Look for parasitized red blood cells.
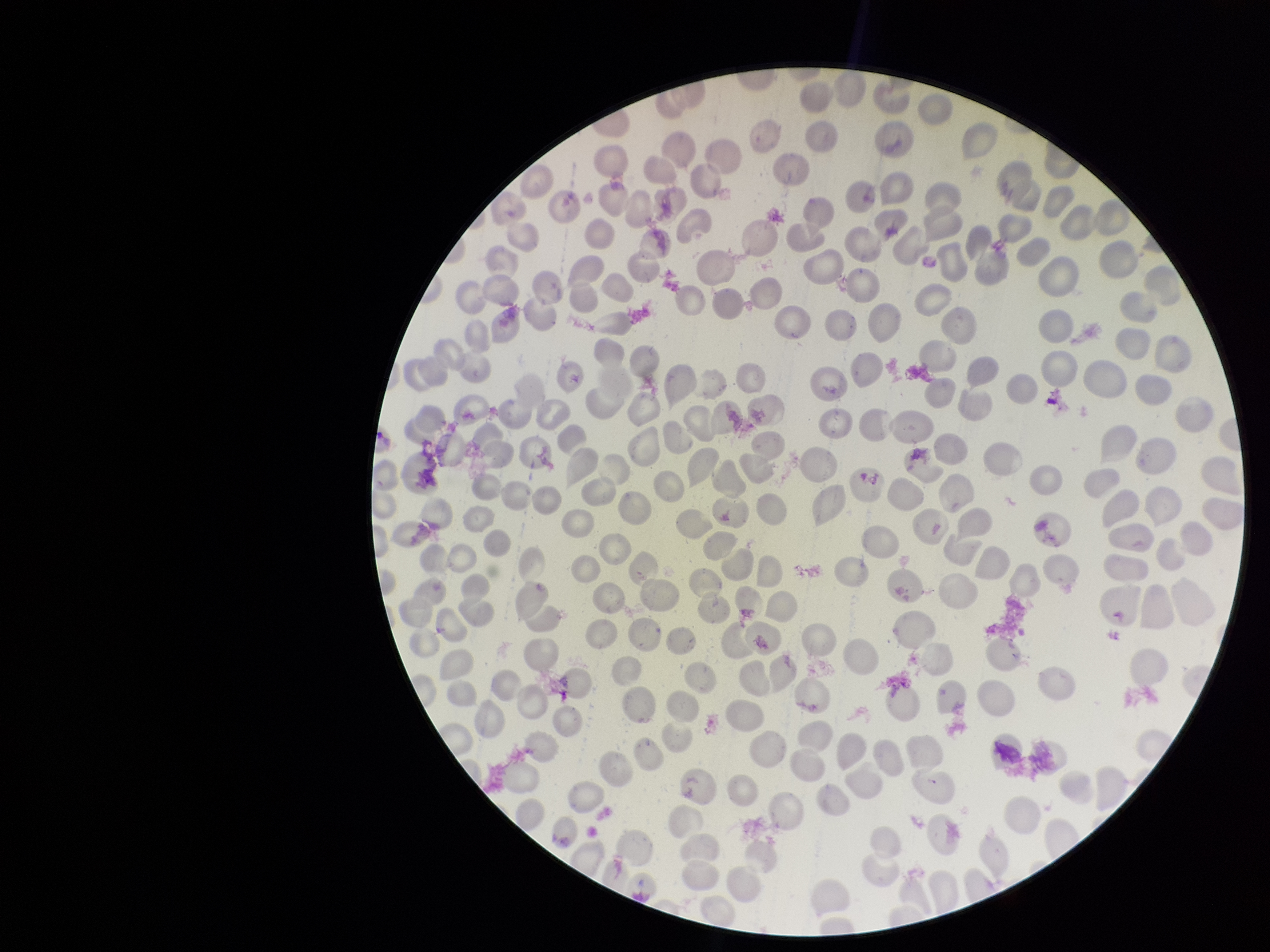

None seen.

stain = Giemsa
preparation = thin blood smear
image size = 1270×952 pixels
patient malaria status = positive
red blood cell count = 268
capture = smartphone photograph through the microscope eyepiece
parasitized red blood cell count = 0
species reported for this patient = Plasmodium vivax
field of view = single